Name the parasite shown.
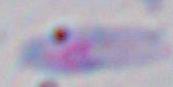

Toxoplasma gondii.

Summary:
  - Modality: micrograph
  - Magnification: 1000x